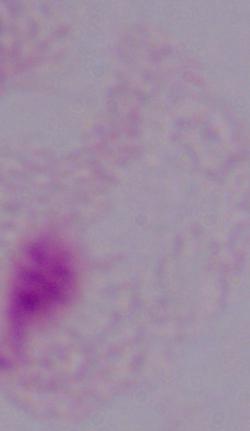 Photomicrograph. A trichomonad is shown. 1000x magnification.